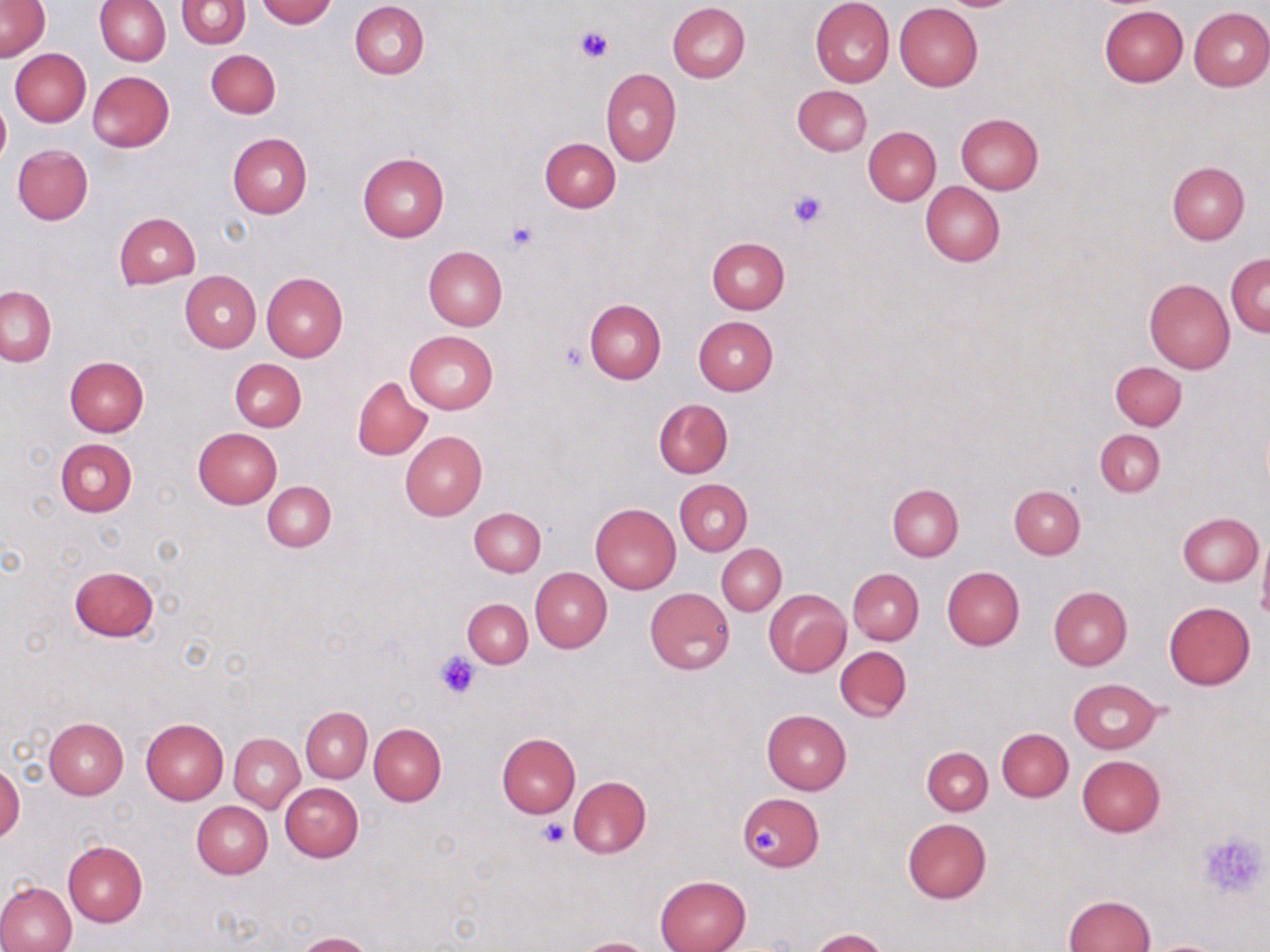
Summary:
  - Coordinate format: approximate bounding boxes as (x1, y1, x2, y2) in pixels
  - Platelet locations: (575, 25, 612, 63), (786, 189, 828, 230), (506, 221, 538, 255), (560, 343, 588, 372), (434, 650, 481, 699), (538, 820, 570, 849), (752, 824, 780, 855), (1198, 831, 1269, 900)
  - Uninfected red blood cell locations: (1, 0, 49, 63), (95, 0, 170, 65), (257, 0, 335, 26), (811, 0, 894, 87), (176, 1, 249, 48), (350, 1, 429, 79), (667, 2, 750, 82), (894, 3, 983, 91), (1100, 6, 1187, 86), (1188, 6, 1270, 91), (10, 48, 91, 127), (206, 49, 280, 118), (601, 68, 681, 165), (88, 71, 174, 151), (791, 84, 872, 156), (0, 99, 9, 168), (955, 113, 1044, 194), (863, 127, 940, 205), (227, 133, 312, 218), (540, 137, 620, 213), (12, 144, 93, 225), (357, 152, 449, 241), (1167, 161, 1250, 244), (921, 182, 1004, 267), (114, 212, 200, 290), (707, 238, 789, 313), (423, 246, 506, 332), (1225, 252, 1270, 336), (180, 271, 261, 352), (262, 273, 348, 361), (1144, 278, 1235, 374), (1, 286, 55, 366), (584, 299, 666, 384), (693, 315, 778, 396), (404, 330, 498, 414), (65, 356, 148, 437), (230, 358, 305, 431), (1110, 362, 1186, 430), (352, 375, 432, 460), (654, 399, 733, 478), (192, 428, 282, 508), (1095, 430, 1165, 497), (400, 431, 487, 518), (55, 438, 137, 516), (674, 479, 752, 556), (263, 481, 335, 552), (888, 483, 963, 561), (1009, 484, 1084, 559), (590, 503, 681, 595), (469, 508, 545, 576), (1177, 512, 1262, 586), (1257, 535, 1270, 627), (717, 544, 786, 615), (69, 565, 160, 642), (943, 566, 1024, 650), (531, 567, 611, 652), (848, 568, 924, 645), (644, 587, 735, 675), (1049, 587, 1132, 670), (764, 590, 851, 676), (462, 599, 533, 668), (1164, 602, 1255, 690), (835, 645, 911, 721), (1067, 679, 1163, 754), (301, 707, 372, 782), (762, 710, 851, 795), (43, 717, 129, 798), (141, 718, 228, 805), (369, 724, 446, 806), (997, 728, 1073, 801), (229, 733, 304, 812), (496, 733, 580, 817), (922, 747, 992, 815), (1077, 755, 1165, 837), (0, 760, 23, 845), (566, 775, 651, 858), (280, 783, 363, 861), (738, 794, 822, 871), (191, 801, 273, 878), (902, 818, 991, 903), (63, 841, 148, 927), (656, 875, 750, 952), (0, 881, 76, 952), (1063, 895, 1154, 952), (809, 928, 888, 952), (296, 931, 376, 952), (572, 937, 657, 952), (1146, 939, 1228, 952)
  - Slide-level diagnosis: negative for blood parasites
  - Modality: light microscopy
  - Magnification: 1000x
  - Preparation: thin blood film
  - Stain: May-Grünwald-Giemsa
  - Field of view: single
  - Image size: 1270×952 pixels